Assess the morphology of the erythrocytes.
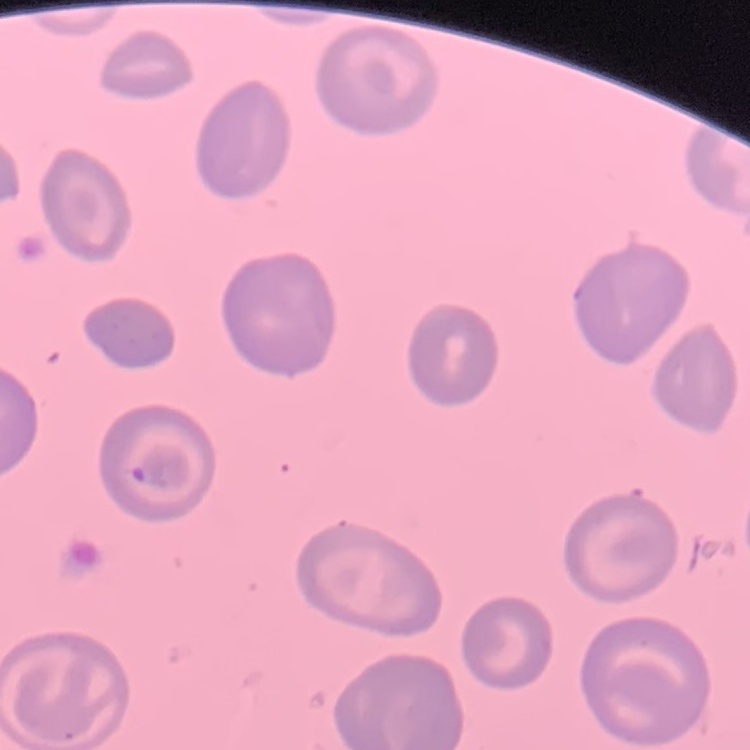
They show no rouleaux formation.

One tile cut from a larger photomicrograph. Field's or Giemsa stain. Thin blood smear.